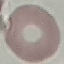
Malaria status: uninfected. Automatically extracted cell patch, resized to 64 × 64 pixels. Giemsa-stained preparation. Acquired by smartphone through the microscope eyepiece. Thin blood film.